Locate platelets.
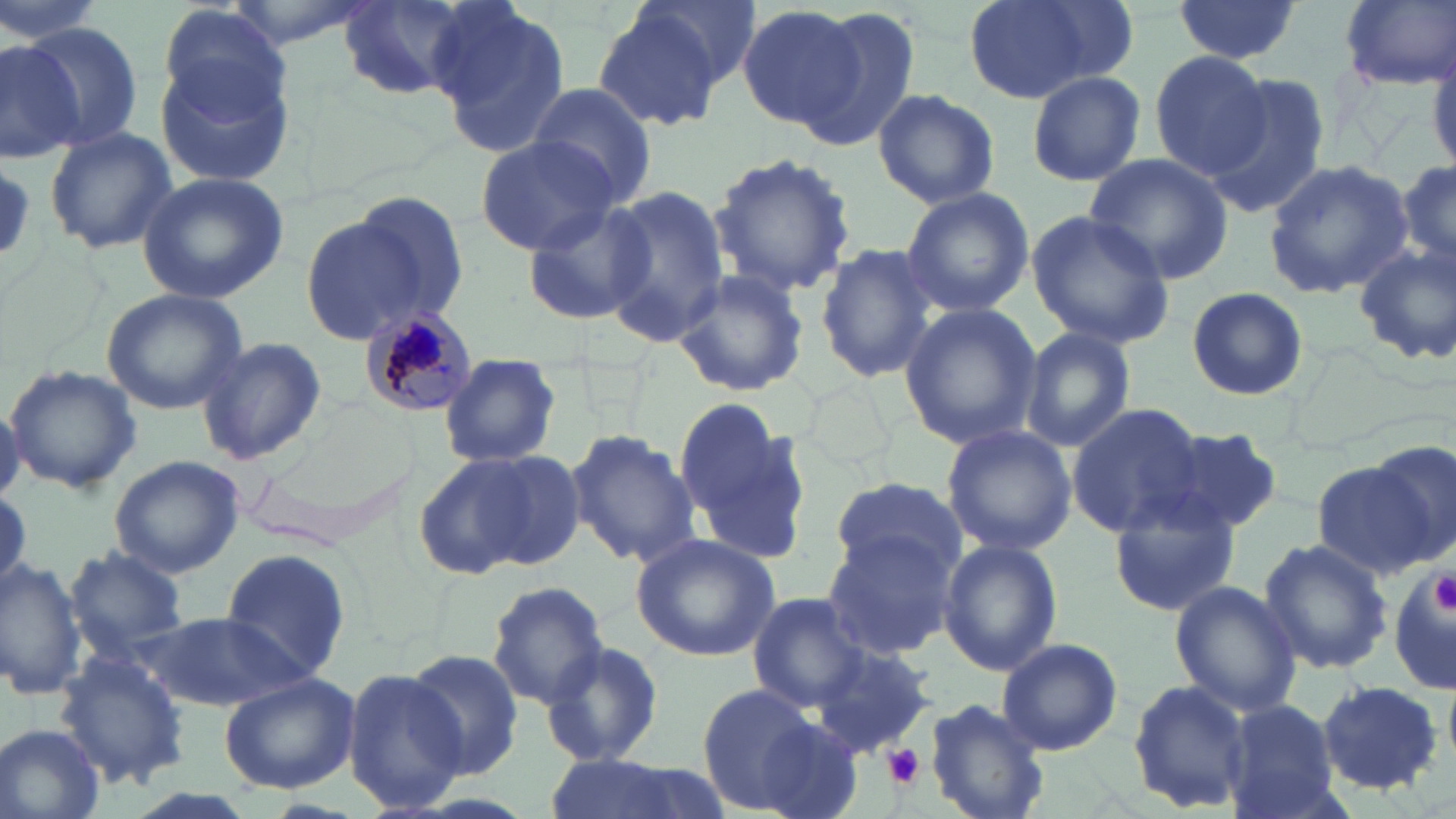
Approximate bounding boxes as [x1, y1, x2, y2] in pixels.
Platelets: [1430, 573, 1456, 613], [884, 744, 924, 788].

Plasmodium malariae-infected red blood cell locations: [361, 307, 478, 416]. Uninfected red blood cell locations: [0, 0, 110, 45], [218, 0, 380, 48], [635, 0, 761, 89], [962, 0, 1126, 104], [1170, 0, 1303, 65], [1338, 0, 1456, 89], [339, 1, 480, 103], [426, 1, 573, 158], [155, 4, 292, 120], [735, 5, 866, 131], [794, 6, 920, 153], [592, 12, 726, 133], [21, 23, 144, 150], [0, 39, 85, 160], [1148, 49, 1273, 180], [155, 52, 296, 190], [1023, 68, 1147, 187], [1202, 77, 1331, 218], [526, 81, 659, 207], [871, 88, 1002, 208], [43, 123, 178, 257], [477, 135, 622, 253], [708, 151, 856, 297], [1082, 153, 1233, 285], [1396, 154, 1455, 282], [1263, 157, 1414, 299], [136, 172, 290, 303], [602, 186, 729, 345], [901, 187, 1034, 317], [347, 189, 469, 325], [523, 202, 658, 326], [1024, 209, 1176, 349], [295, 211, 438, 342], [815, 242, 940, 383], [1352, 243, 1456, 367], [670, 270, 811, 397], [1184, 286, 1310, 401], [101, 288, 247, 415], [897, 302, 1042, 449], [1019, 324, 1140, 452], [194, 336, 327, 467], [440, 354, 560, 466], [4, 363, 143, 493], [675, 399, 807, 556], [1065, 403, 1207, 537], [0, 404, 23, 503], [941, 424, 1077, 555], [564, 429, 699, 568], [1161, 429, 1287, 535], [1367, 439, 1456, 569], [415, 450, 570, 579], [108, 454, 245, 579], [1312, 459, 1436, 576], [829, 478, 968, 583], [1107, 492, 1242, 617], [820, 531, 958, 661], [630, 533, 781, 661], [1258, 536, 1393, 675], [938, 537, 1062, 676], [66, 548, 189, 656], [219, 548, 356, 686], [0, 555, 85, 697], [1388, 566, 1456, 696], [1169, 580, 1301, 715], [487, 581, 610, 709], [752, 592, 873, 711], [139, 609, 307, 713], [995, 638, 1123, 756], [542, 641, 664, 767], [807, 644, 938, 761], [402, 647, 522, 777], [50, 650, 192, 791], [342, 667, 468, 812], [216, 673, 359, 792], [1128, 678, 1252, 814], [1315, 679, 1446, 794], [693, 684, 848, 816], [925, 698, 1051, 819], [1221, 701, 1342, 819], [1, 725, 107, 819], [543, 753, 720, 819]. Slide-level diagnosis: Plasmodium malariae. One field of a larger specimen. Thin blood smear. Optical microscopy. May-Grünwald-Giemsa-stained preparation. Image is 1456×819 pixels. 1000x magnification.